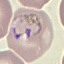
{
  "result": "malaria parasites detected",
  "preparation": "thin smear",
  "stain": "Giemsa",
  "image_type": "automatically extracted cell patch, resized to 64 × 64 pixels",
  "capture": "smartphone camera at the microscope eyepiece"
}